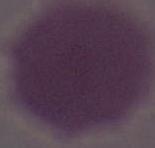
{
  "identification": "red blood cell",
  "magnification": "1000x",
  "modality": "photomicrograph"
}